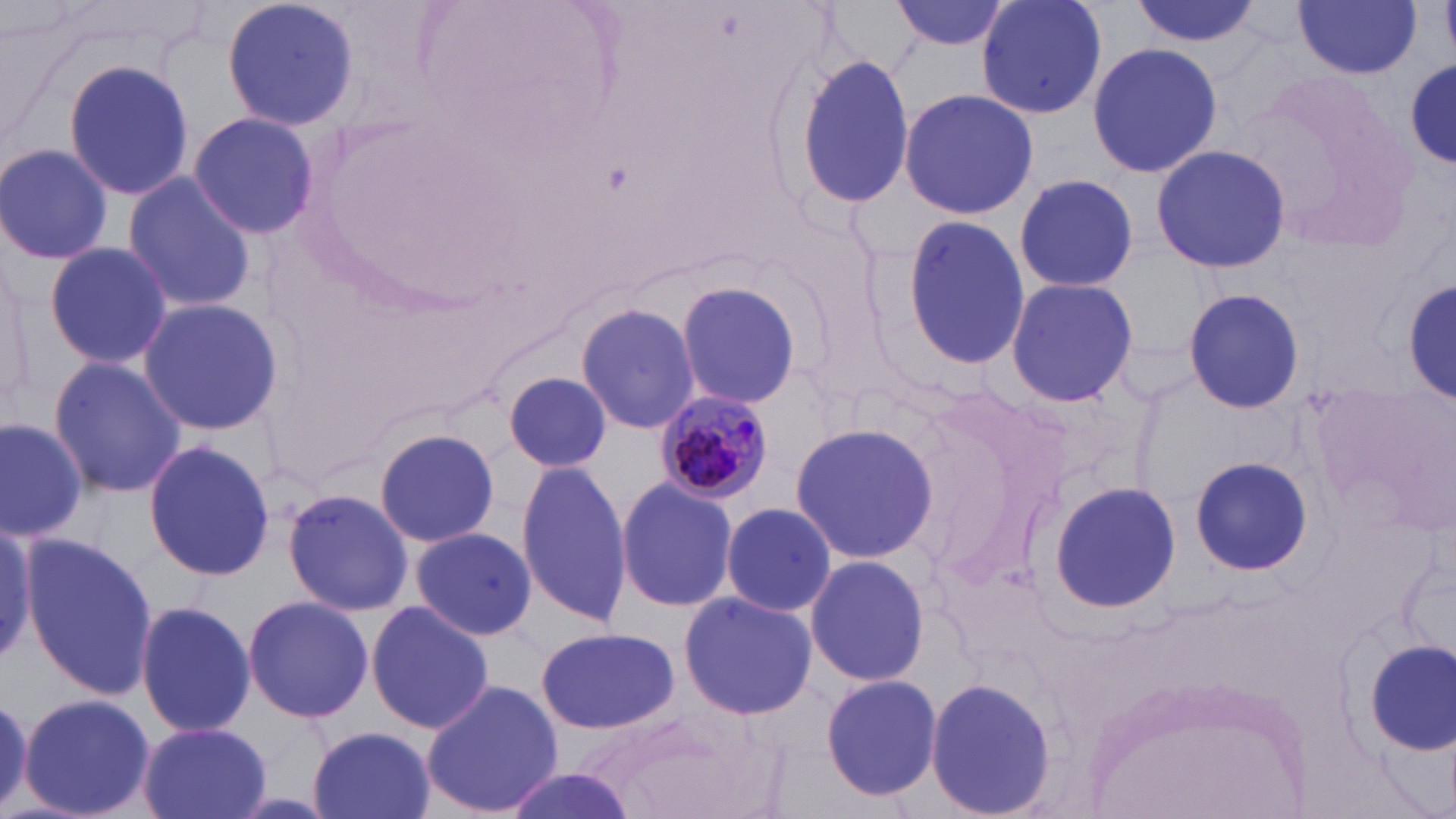
Approximate bounding boxes as named x1/y1/x2/y2 corners in pixels. Uninfected red blood cell locations: (x1=221, y1=0, x2=360, y2=133), (x1=977, y1=0, x2=1106, y2=121), (x1=1130, y1=0, x2=1262, y2=49), (x1=1293, y1=0, x2=1421, y2=78), (x1=891, y1=1, x2=1013, y2=52), (x1=1087, y1=42, x2=1222, y2=178), (x1=791, y1=52, x2=915, y2=213), (x1=63, y1=58, x2=193, y2=203), (x1=1407, y1=61, x2=1456, y2=170), (x1=1237, y1=67, x2=1413, y2=248), (x1=899, y1=88, x2=1037, y2=219), (x1=190, y1=112, x2=320, y2=240), (x1=0, y1=142, x2=117, y2=266), (x1=1151, y1=143, x2=1290, y2=275), (x1=121, y1=172, x2=258, y2=313), (x1=1012, y1=173, x2=1139, y2=291), (x1=899, y1=215, x2=1028, y2=371), (x1=43, y1=240, x2=173, y2=369), (x1=1, y1=271, x2=34, y2=417), (x1=1004, y1=276, x2=1138, y2=407), (x1=672, y1=277, x2=805, y2=410), (x1=1404, y1=278, x2=1456, y2=402), (x1=1182, y1=285, x2=1306, y2=414), (x1=136, y1=298, x2=282, y2=434), (x1=574, y1=302, x2=700, y2=434), (x1=47, y1=355, x2=188, y2=500), (x1=504, y1=370, x2=614, y2=474), (x1=0, y1=417, x2=87, y2=541), (x1=792, y1=419, x2=937, y2=565), (x1=375, y1=427, x2=502, y2=547), (x1=143, y1=440, x2=275, y2=580), (x1=1188, y1=456, x2=1313, y2=576), (x1=515, y1=461, x2=629, y2=624), (x1=615, y1=476, x2=739, y2=613), (x1=1046, y1=481, x2=1181, y2=613), (x1=283, y1=488, x2=412, y2=616), (x1=719, y1=504, x2=840, y2=619), (x1=0, y1=524, x2=41, y2=665), (x1=410, y1=526, x2=537, y2=642), (x1=21, y1=534, x2=155, y2=700), (x1=804, y1=555, x2=929, y2=686), (x1=678, y1=591, x2=817, y2=720), (x1=241, y1=595, x2=374, y2=723), (x1=134, y1=599, x2=256, y2=738), (x1=367, y1=600, x2=493, y2=736), (x1=536, y1=625, x2=679, y2=735), (x1=1364, y1=639, x2=1456, y2=753), (x1=820, y1=672, x2=942, y2=803), (x1=923, y1=676, x2=1056, y2=819), (x1=422, y1=678, x2=563, y2=818), (x1=18, y1=693, x2=155, y2=819), (x1=0, y1=694, x2=34, y2=813), (x1=582, y1=709, x2=752, y2=817), (x1=137, y1=723, x2=271, y2=819), (x1=305, y1=725, x2=437, y2=819), (x1=498, y1=766, x2=642, y2=819). Plasmodium malariae-infected red blood cell locations: (x1=653, y1=387, x2=776, y2=503). Slide-level diagnosis: Plasmodium malariae. Image is 1456×819 pixels. May-Grünwald-Giemsa stain. Thin blood smear. One field of a larger specimen. Optical microscopy. Captured at 1000x magnification.